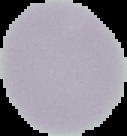

preparation = thin blood smear
malaria status = uninfected
image size = 127×136 pixels
image type = cell region segmented out of the field of view; surrounding area masked to black